Name the cell type shown.
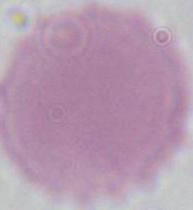
An erythrocyte.

Summary:
  - Magnification: 1000x
  - Modality: micrograph